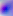

identification = Toxoplasma gondii
modality = micrograph
magnification = 400x